Assess this cell for malaria.
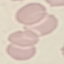
Uninfected.

Thin blood smear. Giemsa-stained preparation. Automatically extracted cell patch, resized to 64 × 64 pixels. Photographed with a smartphone camera at the microscope eyepiece.